Outline each Plasmodium vivax-infected red blood cell.
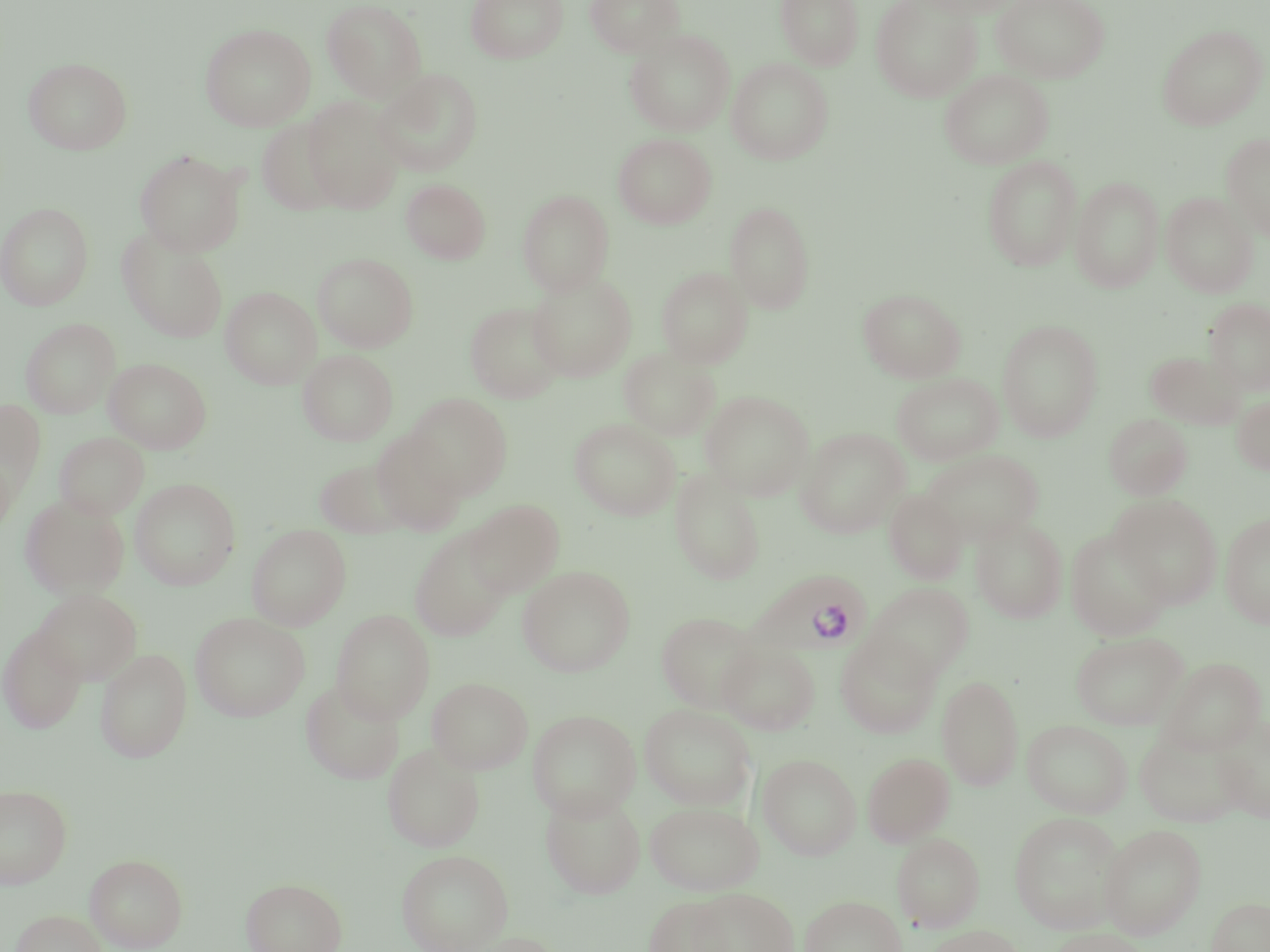
Approximate bounding boxes as [x1, y1, x2, y2] in pixels.
Plasmodium vivax-infected red blood cells: [748, 569, 873, 658].

Uninfected red blood cell locations: [315, 0, 414, 209], [321, 0, 428, 101], [466, 0, 568, 64], [584, 0, 685, 57], [776, 0, 863, 69], [870, 0, 982, 101], [910, 0, 1022, 18], [991, 0, 1110, 83], [200, 23, 315, 131], [1157, 24, 1267, 130], [624, 29, 736, 136], [23, 56, 133, 155], [726, 58, 833, 164], [374, 68, 483, 176], [939, 69, 1054, 169], [301, 97, 404, 212], [256, 118, 346, 215], [613, 133, 716, 229], [1221, 133, 1270, 242], [135, 149, 246, 256], [982, 156, 1082, 272], [1071, 176, 1164, 292], [401, 179, 491, 264], [517, 189, 615, 295], [1161, 192, 1258, 297], [725, 200, 816, 313], [0, 201, 94, 310], [116, 227, 228, 342], [313, 252, 418, 352], [656, 267, 753, 368], [527, 273, 637, 382], [220, 286, 321, 389], [858, 288, 966, 383], [1205, 298, 1270, 393], [465, 301, 567, 403], [21, 318, 120, 418], [997, 319, 1103, 441], [619, 348, 720, 440], [298, 349, 397, 445], [1145, 350, 1245, 430], [104, 358, 211, 453], [892, 372, 1004, 465], [700, 390, 815, 500], [405, 393, 513, 498], [1233, 395, 1270, 475], [0, 400, 45, 503], [1104, 414, 1192, 499], [570, 418, 681, 521], [796, 427, 909, 537], [370, 429, 468, 535], [54, 432, 149, 520], [922, 449, 1044, 545], [314, 458, 414, 538], [670, 468, 766, 585], [130, 478, 241, 590], [884, 489, 968, 585], [1110, 494, 1223, 608], [20, 495, 129, 599], [464, 499, 565, 597], [1220, 513, 1270, 629], [970, 516, 1068, 623], [246, 524, 351, 630], [409, 528, 513, 641], [1065, 528, 1172, 641], [517, 566, 635, 676], [867, 582, 975, 681], [34, 589, 142, 685], [331, 609, 435, 723], [656, 611, 762, 713], [190, 612, 310, 721], [0, 624, 87, 733], [1071, 632, 1188, 730], [835, 634, 942, 739], [717, 640, 820, 734], [95, 648, 192, 763], [1159, 657, 1267, 755], [937, 675, 1024, 790], [427, 676, 533, 774], [300, 679, 405, 785], [639, 704, 756, 809], [527, 709, 641, 820], [1213, 713, 1270, 823], [1022, 719, 1132, 817], [1134, 726, 1245, 828], [382, 742, 484, 851], [758, 753, 861, 859], [862, 753, 955, 846], [0, 785, 72, 888], [540, 788, 646, 899], [645, 800, 764, 894], [1009, 812, 1126, 932], [1099, 824, 1206, 939], [891, 833, 985, 931], [396, 849, 513, 952], [85, 853, 188, 952], [241, 877, 347, 952], [689, 888, 798, 952], [800, 895, 906, 952], [643, 896, 734, 952], [1205, 896, 1270, 952], [9, 909, 109, 952], [924, 925, 1025, 952], [1047, 928, 1149, 952]. Slide-level diagnosis: Plasmodium vivax. Thin blood smear. Optical microscopy. One field of a larger specimen. May-Grünwald-Giemsa-stained preparation. Image is 1270×952 pixels. 1000x magnification.